Point out each Plasmodium parasite.
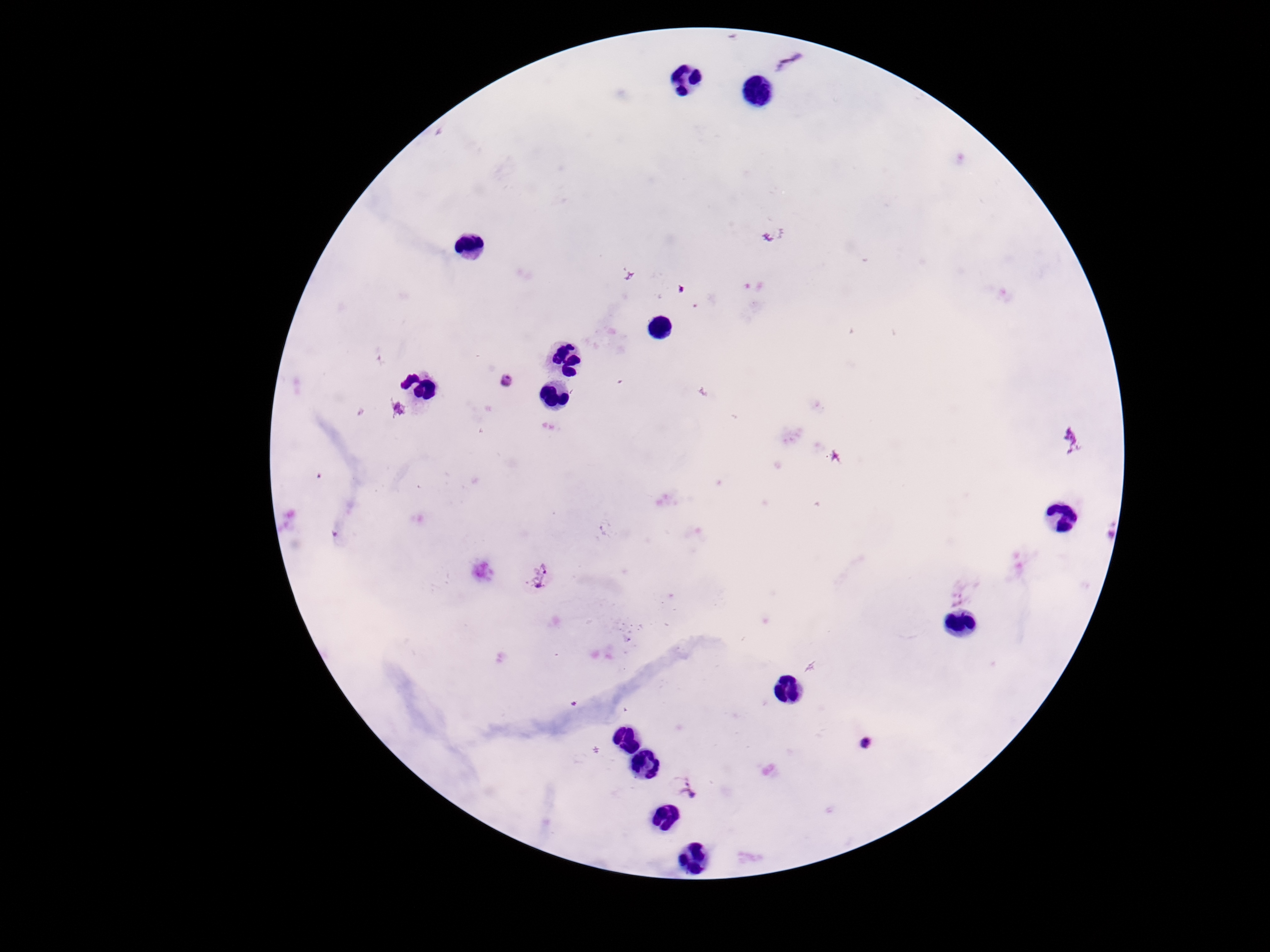

Approximate centers as [x, y] in pixels.
Plasmodium parasites: [788, 62], [509, 380], [395, 410], [1071, 438], [541, 574], [963, 591], [867, 742], [691, 786].

magnification = 100x
preparation = thick blood film
image size = 1270×952 pixels
stain = Giemsa
patient malaria status = positive
capture = smartphone camera through the microscope eyepiece
field of view = one from this slide